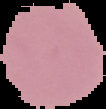
image_type: cell region segmented out of the field of view; surrounding area masked to black
image_size: 106×109 pixels
preparation: thin blood smear
malaria_status: uninfected